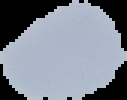
{
  "image_type": "segmented cell region on a black background",
  "image_size": "127×100 pixels",
  "preparation": "thin blood film",
  "result": "no Plasmodium parasites detected"
}